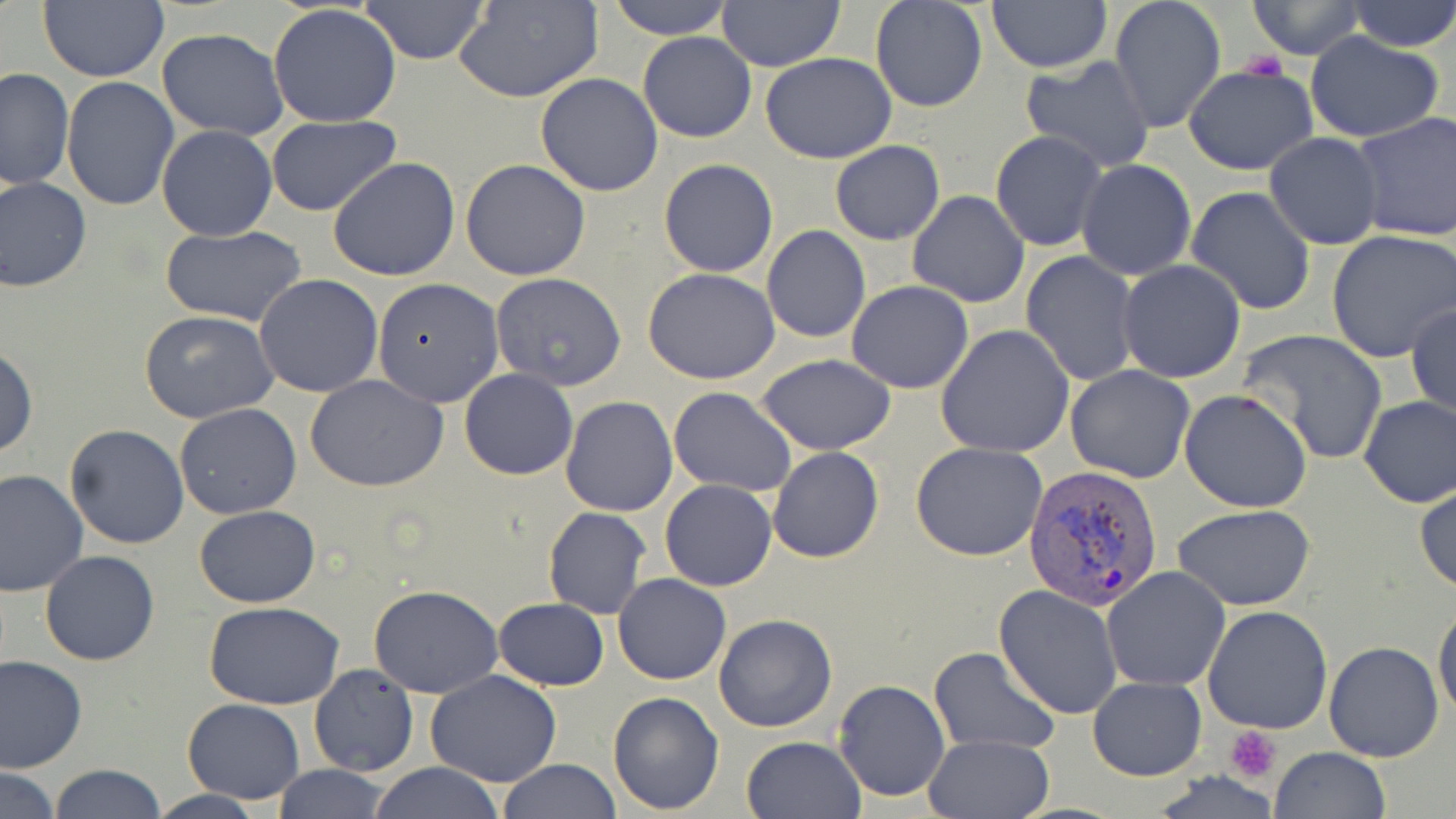
Summary:
  - Coordinate format: approximate bounding boxes as [x1, y1, x2, y2] in pixels
  - Plasmodium vivax-infected red blood cell locations: [1025, 463, 1164, 610]
  - Uninfected red blood cell locations: [38, 0, 168, 82], [607, 0, 734, 40], [716, 0, 843, 70], [869, 0, 989, 113], [987, 0, 1111, 73], [1109, 0, 1226, 133], [1248, 0, 1366, 58], [1344, 0, 1456, 52], [359, 1, 490, 64], [457, 1, 602, 104], [267, 5, 402, 129], [157, 28, 290, 141], [639, 31, 756, 143], [1304, 31, 1445, 142], [760, 53, 897, 164], [1018, 54, 1156, 174], [1182, 62, 1319, 175], [2, 66, 76, 191], [536, 73, 663, 197], [61, 75, 179, 211], [1351, 110, 1456, 242], [265, 114, 402, 217], [155, 125, 277, 242], [991, 129, 1107, 251], [1264, 131, 1383, 249], [830, 140, 945, 245], [327, 158, 460, 281], [658, 158, 779, 278], [460, 159, 590, 281], [1076, 159, 1196, 280], [0, 176, 93, 293], [1185, 187, 1314, 316], [907, 190, 1030, 308], [162, 226, 306, 327], [761, 226, 871, 343], [1327, 229, 1456, 362], [1021, 251, 1142, 386], [1117, 259, 1247, 384], [644, 269, 782, 385], [490, 272, 627, 391], [254, 274, 384, 397], [372, 279, 504, 409], [847, 281, 973, 392], [1406, 302, 1455, 423], [140, 309, 278, 422], [936, 325, 1074, 459], [1239, 329, 1388, 465], [0, 343, 38, 460], [756, 355, 898, 453], [1066, 365, 1196, 484], [459, 368, 578, 480], [307, 376, 447, 492], [668, 387, 798, 496], [1179, 390, 1312, 514], [559, 395, 677, 516], [1358, 395, 1456, 507], [174, 402, 302, 520], [64, 423, 192, 550], [911, 442, 1048, 562], [768, 448, 884, 563], [0, 469, 89, 595], [1415, 474, 1456, 595], [659, 478, 777, 592], [194, 504, 320, 609], [1173, 505, 1319, 611], [543, 508, 651, 619], [40, 549, 160, 665], [1104, 566, 1231, 692], [614, 573, 731, 684], [368, 585, 505, 699], [994, 585, 1122, 720], [493, 598, 608, 690], [1432, 600, 1455, 724], [203, 601, 345, 710], [1202, 605, 1333, 735], [713, 613, 837, 732], [1324, 640, 1444, 761], [928, 646, 1060, 753], [0, 656, 87, 772], [310, 664, 418, 777], [426, 671, 563, 787], [1087, 677, 1207, 781], [834, 679, 949, 802], [607, 691, 724, 813], [181, 698, 306, 802], [923, 733, 1055, 819], [741, 734, 867, 819], [1268, 747, 1390, 819], [497, 759, 621, 818], [367, 763, 505, 819], [50, 764, 165, 819], [273, 764, 390, 819], [1, 767, 62, 819], [1151, 774, 1282, 816], [145, 789, 265, 819]
  - Platelet locations: [1240, 52, 1287, 83], [1226, 726, 1283, 780]
  - Slide-level diagnosis: Plasmodium vivax
  - Magnification: 1000x
  - Image size: 1456×819 pixels
  - Stain: May-Grünwald-Giemsa
  - Field of view: single
  - Preparation: thin blood smear
  - Modality: light microscopy